Look for Plasmodium parasites.
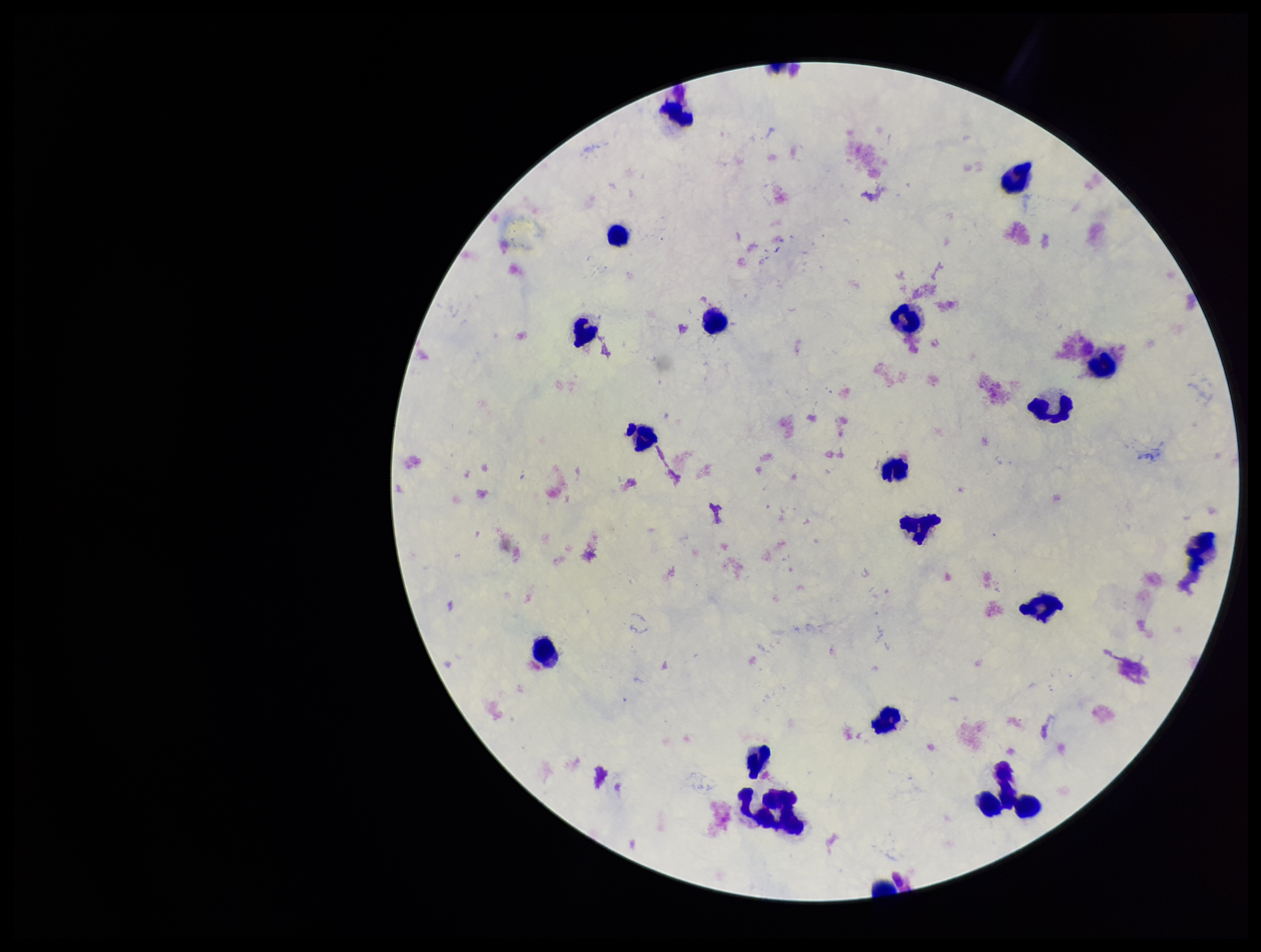
None identified.

image size = 1261×952 pixels
field of view = single
leukocyte count = 20
patient malaria status = negative
stain = Giemsa
preparation = thick smear
parasite count = 0
capture = smartphone photograph through the microscope eyepiece